Assess this cell for malaria.
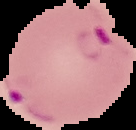

Parasitized.

Image is 136×130 pixels. From a thin blood film. Cell region segmented out of the field of view; the surrounding area is masked to black.